Assess the morphology of the erythrocytes.
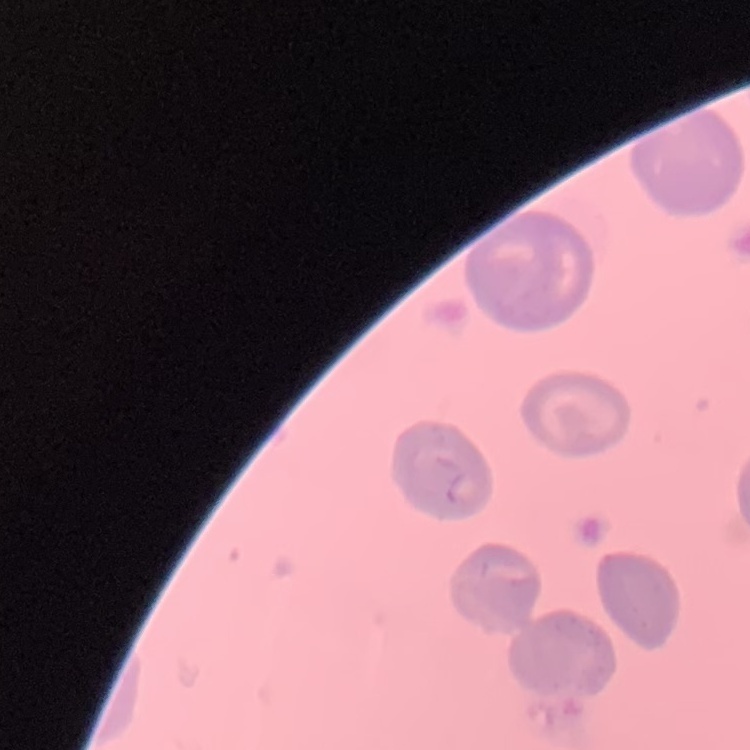

They show no rouleaux formation.

Stained with either Field's or Giemsa. Thin blood film. Square crop of a larger photomicrograph.